Identify the preparation type.
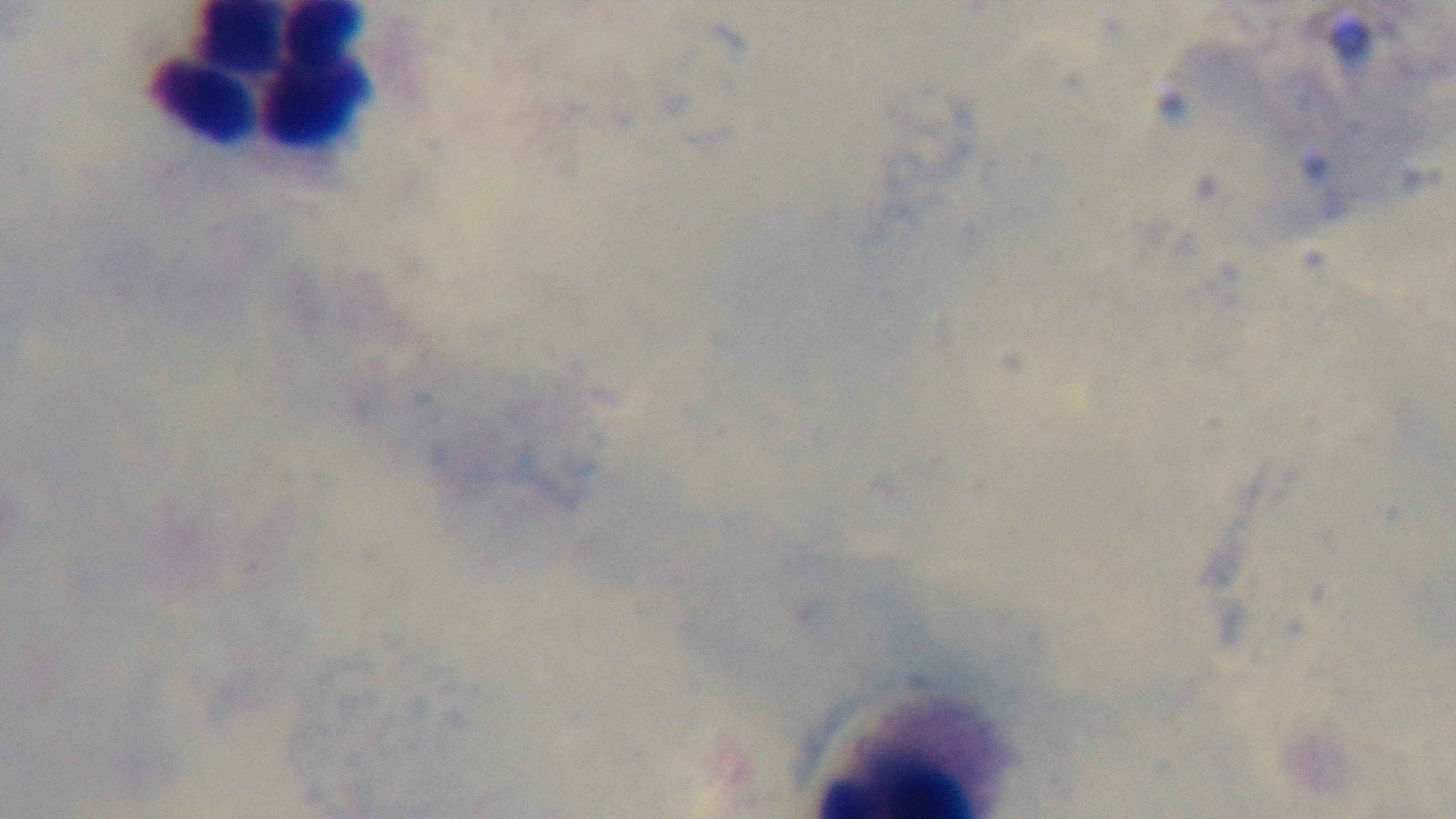
A thick smear.

{
  "stain": "Giemsa",
  "field_of_view": "one from the slide",
  "modality": "light microscopy",
  "malaria_status": "uninfected",
  "objective": "100x oil immersion",
  "capture": "mounted 4K digital camera"
}